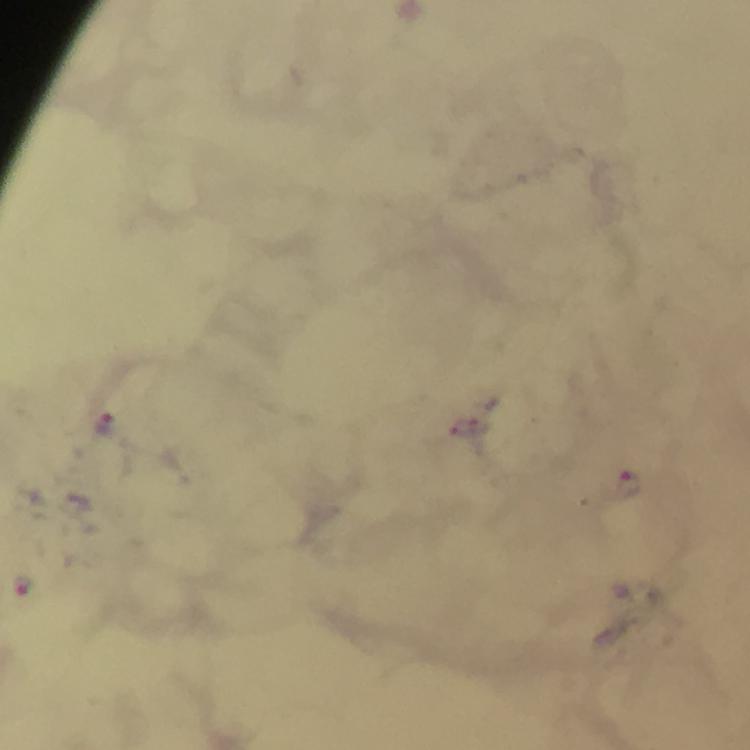

Approximate centers as {x, y} in pixels.
Summary:
  - Malaria parasite locations: {106, 426}, {629, 484}, {23, 585}
  - Immersion oil: applied
  - Cropped from: one field of view
  - Context: from a diagnostic examination for malaria
  - Magnification: 100x
  - Capture: smartphone photograph through a microscope
  - Preparation: thick blood film
  - Stain: Giemsa
  - Image size: 750×750 pixels